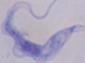
modality = micrograph
magnification = 1000x
identification = trypanosome